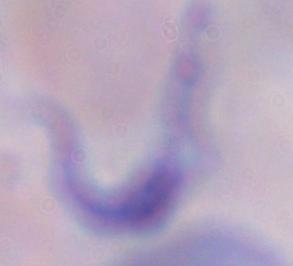
{
  "magnification": "1000x",
  "identification": "trypanosome",
  "modality": "micrograph"
}